Assess this cell for malaria.
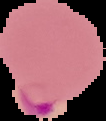

Parasitized.

Image is 106×121 pixels. The area outside the segmented cell region is set to black. From a thin blood smear.